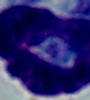

Summary:
  - Magnification: 1000x
  - Identification: leukocyte
  - Modality: photomicrograph